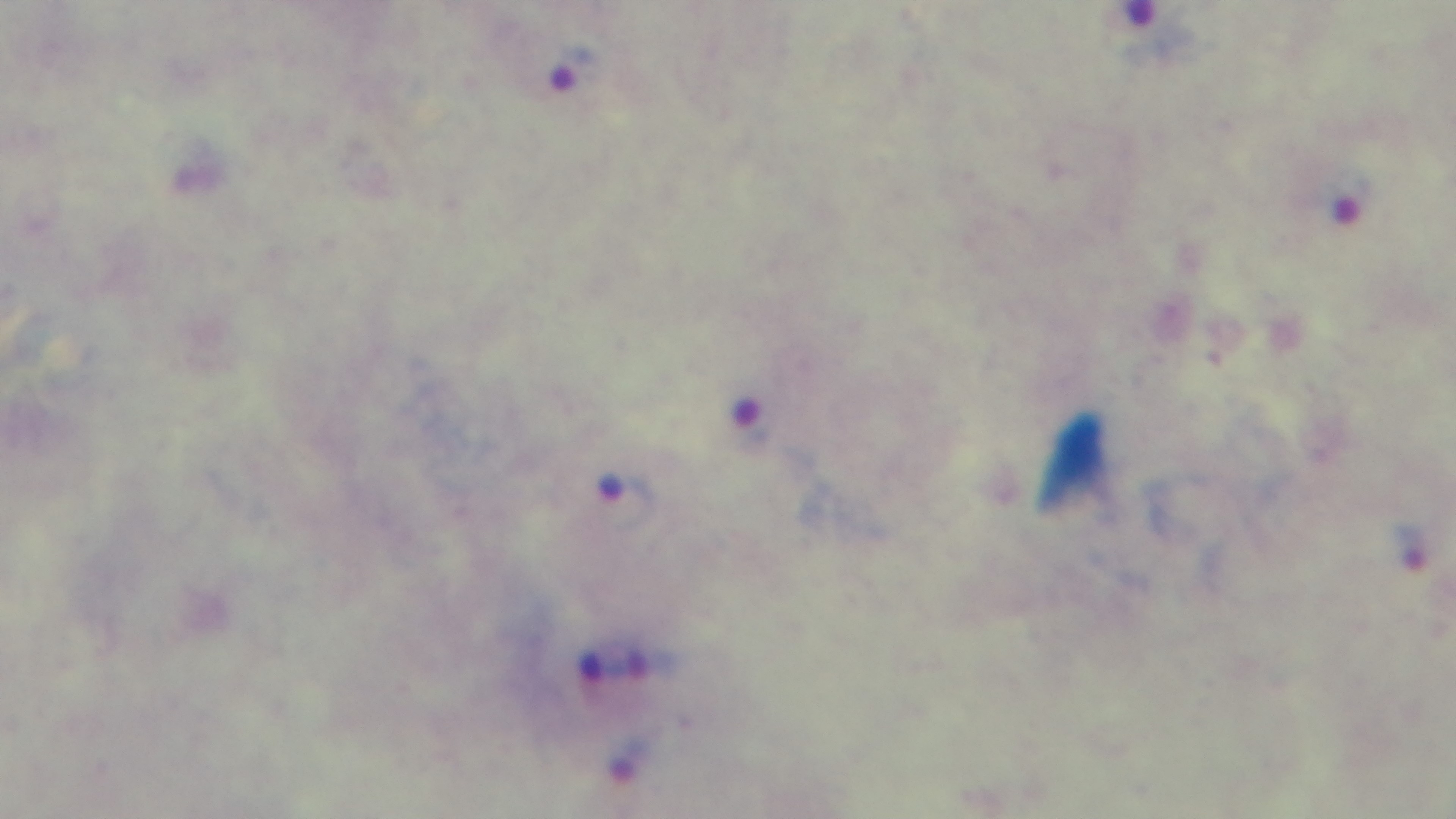

Summary:
  - Field of view: single
  - Capture: mounted 4K digital camera
  - Modality: light microscopy
  - Malaria status: positive
  - Preparation: thick blood film
  - Objective: 100x oil immersion
  - Stain: Giemsa